Give the position of every malaria parasite.
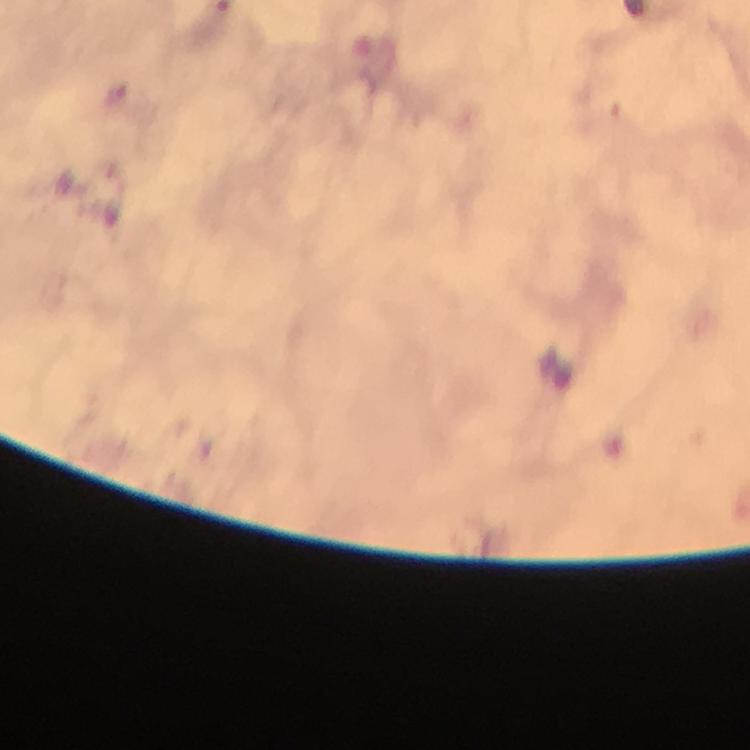

Approximate centers as [x, y] in pixels.
Malaria parasites: [118, 92].

cropped from = a single field of view
context = from a malaria diagnostic workup
image size = 750×750 pixels
immersion oil = used
preparation = thick smear
magnification = 100x
capture = smartphone camera through the microscope
stain = Giemsa